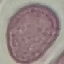

result: no malaria parasites detected
capture: smartphone camera at the microscope eyepiece
stain: Giemsa
image_type: cell patch, automatically extracted from a larger field of view and resized to 64 × 64 pixels
preparation: thin blood film